Assess the morphology of the red blood cells.
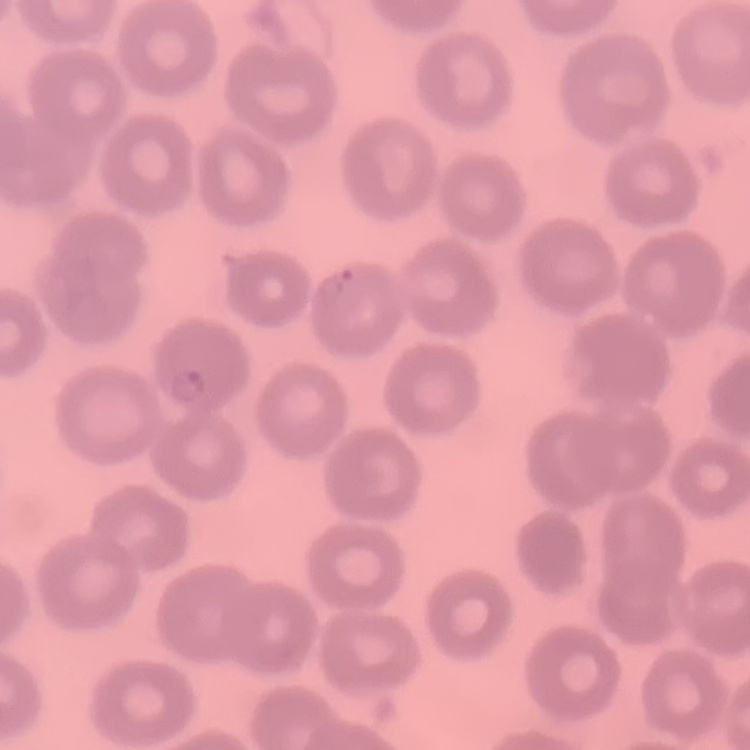
They show no rouleaux formation.

image type = one tile cut from a larger photomicrograph
preparation = thin peripheral smear
stain = Field's or Giemsa